Locate and identify every blood parasite.
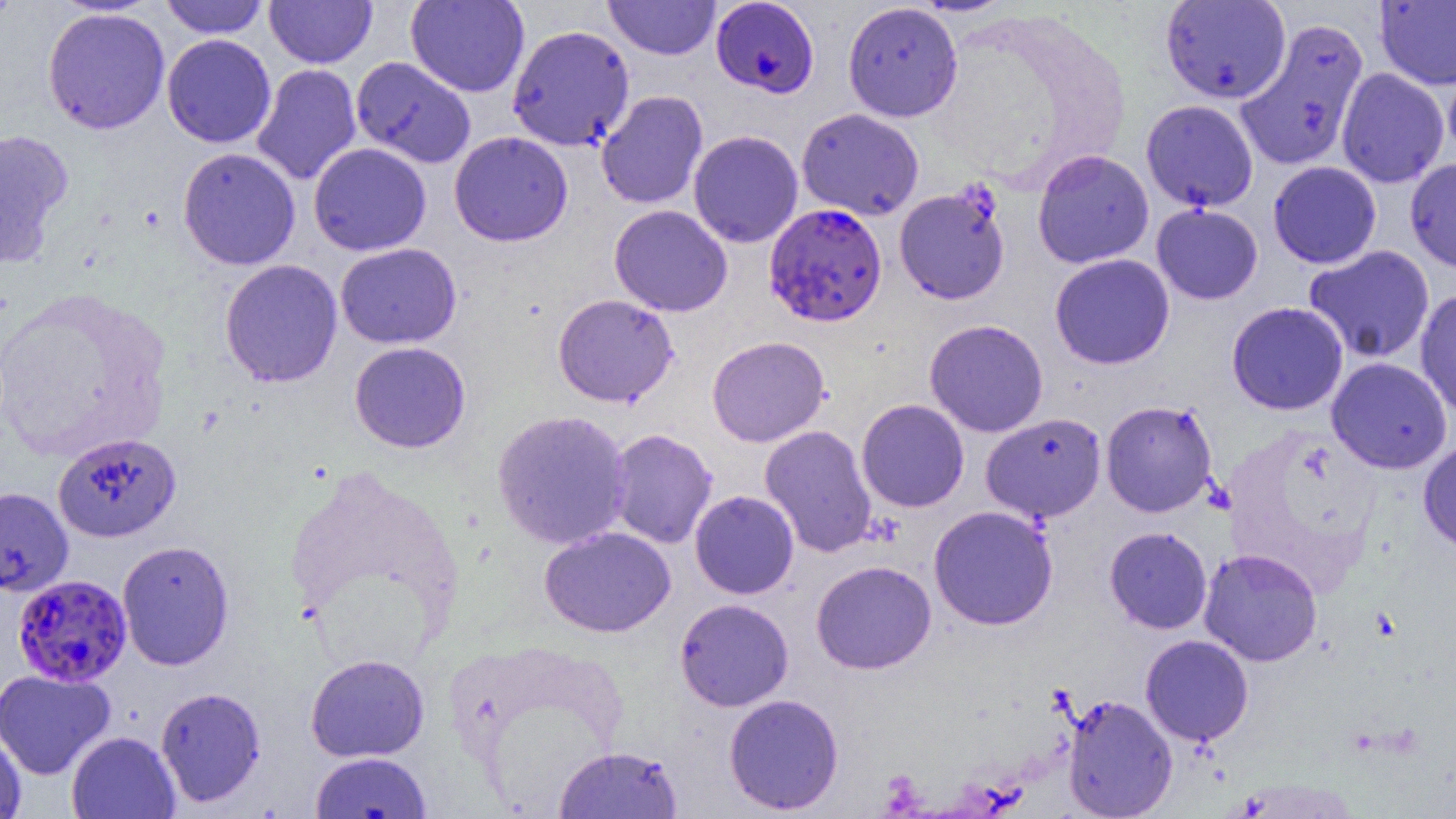

Approximate bounding boxes as (x1, y1, x2, y2) in pixels.
Plasmodium falciparum-infected red blood cells: (711, 1, 819, 98), (764, 203, 887, 327), (13, 574, 133, 687).
No Plasmodium ovale, Plasmodium malariae, Plasmodium vivax, Babesia divergens, or Trypanosoma brucei observed.

Uninfected red blood cell locations: (160, 0, 269, 38), (264, 0, 377, 68), (604, 0, 720, 60), (908, 0, 1017, 16), (1160, 0, 1291, 104), (1375, 0, 1456, 90), (405, 1, 530, 97), (842, 2, 963, 122), (42, 6, 170, 134), (1235, 17, 1370, 172), (507, 24, 635, 151), (162, 34, 276, 148), (351, 56, 476, 169), (251, 63, 361, 186), (1336, 68, 1450, 188), (596, 90, 708, 209), (1141, 100, 1259, 212), (796, 108, 924, 221), (0, 128, 73, 267), (687, 130, 803, 248), (449, 131, 573, 247), (308, 142, 432, 256), (177, 147, 301, 270), (1032, 149, 1155, 269), (1405, 156, 1456, 274), (1268, 161, 1382, 269), (893, 184, 1011, 305), (1151, 203, 1263, 305), (608, 205, 733, 317), (335, 243, 461, 349), (1303, 245, 1435, 363), (1049, 254, 1175, 370), (220, 259, 343, 387), (1415, 288, 1456, 419), (552, 293, 678, 407), (1226, 301, 1349, 416), (924, 319, 1049, 437), (706, 335, 830, 447), (349, 341, 471, 453), (1326, 357, 1452, 474), (856, 399, 970, 512), (1101, 400, 1219, 517), (492, 409, 632, 550), (980, 412, 1107, 524), (759, 425, 877, 558), (606, 429, 718, 549), (52, 432, 181, 543), (1417, 439, 1456, 556), (0, 487, 73, 597), (689, 490, 799, 599), (928, 505, 1058, 630), (539, 526, 676, 638), (1104, 526, 1212, 634), (117, 540, 234, 671), (1199, 548, 1322, 666), (811, 560, 937, 674), (674, 598, 794, 711), (1140, 634, 1254, 746), (305, 653, 430, 762), (0, 668, 115, 780), (155, 686, 266, 808), (724, 693, 844, 815), (1061, 693, 1177, 818), (0, 727, 26, 819), (66, 731, 180, 819), (554, 745, 683, 818), (310, 751, 432, 819). Slide-level diagnosis: Plasmodium falciparum. Light microscopy. One field of a larger specimen. Thin blood smear. Captured at 1000x magnification. Image is 1456×819 pixels.